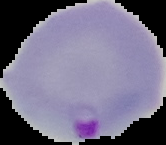 The area outside the segmented cell region is set to black. Result: Plasmodium parasites identified. From a thin blood film. Image is 166×145 pixels.